Classify this cell by malaria status.
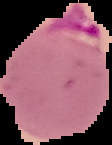

It is parasitized.

{
  "preparation": "thin blood film",
  "image_type": "segmented cell region on a black background",
  "image_size": "112×145 pixels"
}